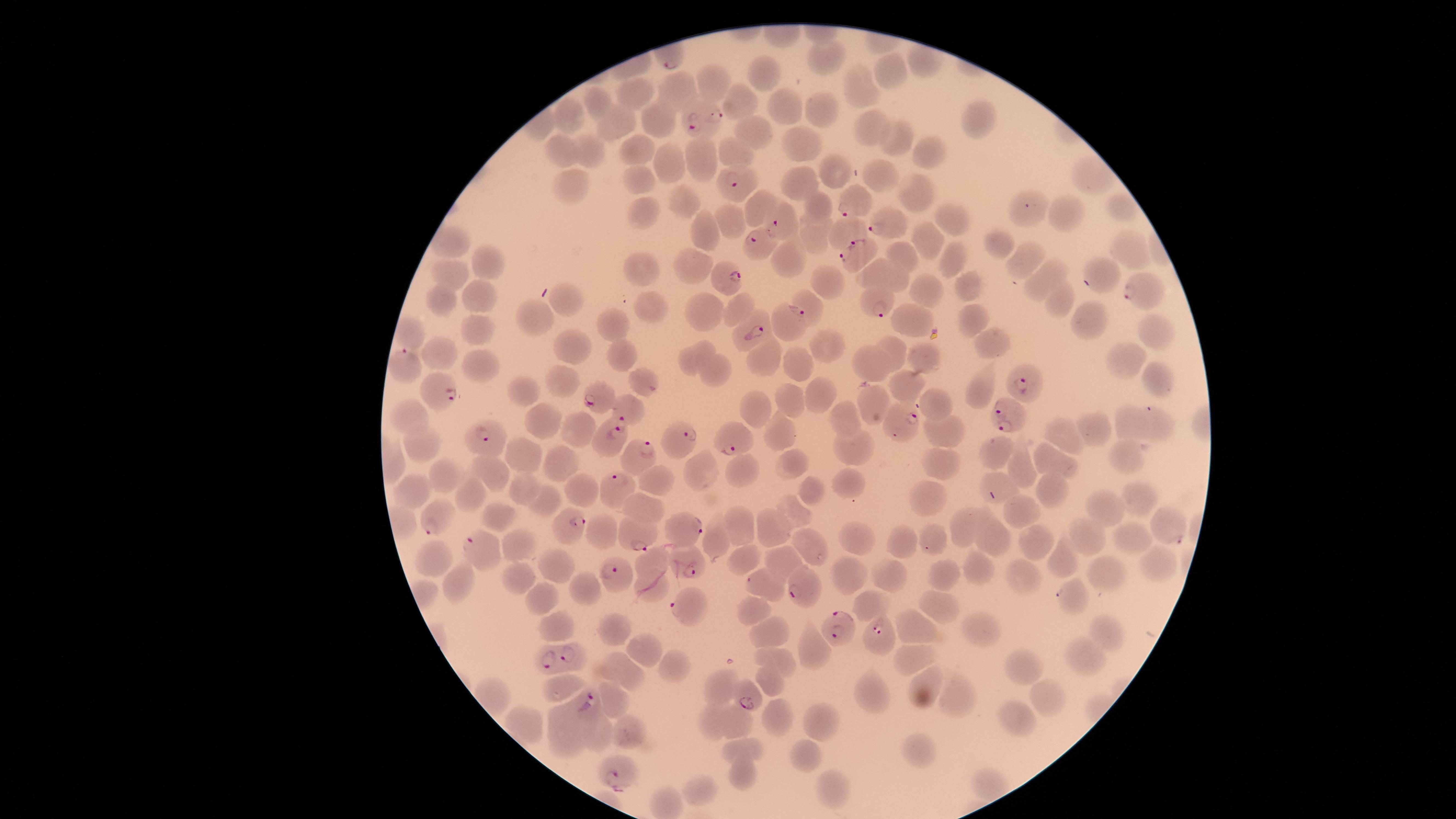 Approximate marker points as [x, y] in pixels. Parasitized RBCs: [703, 124], [738, 178], [850, 202], [783, 225], [887, 226], [755, 238], [857, 249], [728, 276], [1138, 294], [874, 307], [791, 320], [753, 332], [409, 369], [1024, 383], [443, 386], [605, 402], [627, 413], [1003, 419], [902, 420], [613, 435], [733, 439], [487, 440], [684, 442], [641, 457], [618, 482], [436, 521], [567, 524], [690, 531], [1175, 537], [640, 541], [471, 546], [611, 571], [690, 571], [800, 589], [1060, 595], [687, 605], [837, 630], [879, 633], [562, 656], [747, 702], [588, 709], [615, 774]. Uninfected RBCs: [825, 59], [923, 61], [889, 69], [766, 73], [712, 79], [862, 90], [680, 91], [634, 96], [598, 100], [735, 102], [783, 106], [815, 108], [572, 112], [977, 117], [663, 119], [611, 124], [872, 126], [755, 133], [894, 140], [803, 141], [641, 149], [561, 150], [586, 150], [923, 150], [733, 152], [697, 158], [675, 167], [838, 172], [643, 177], [573, 183], [804, 183], [1095, 183], [917, 189], [676, 199], [760, 206], [817, 206], [1121, 210], [1063, 212], [649, 213], [956, 219], [729, 223], [707, 230], [847, 231], [815, 233], [995, 238], [930, 239], [1123, 247], [1022, 252], [789, 253], [903, 255], [951, 257], [492, 261], [697, 265], [1101, 270], [642, 272], [883, 275], [450, 277], [825, 280], [1037, 281], [965, 287], [921, 288], [484, 293], [443, 300], [1050, 300], [569, 301], [809, 304], [701, 307], [742, 307], [649, 311], [974, 318], [1088, 319], [543, 320], [908, 320], [612, 325], [1151, 326], [479, 332], [411, 333], [992, 341], [825, 346], [894, 346], [575, 349], [925, 352], [443, 353], [627, 357], [691, 359], [765, 361], [1124, 361], [869, 364], [796, 365], [479, 367], [713, 371], [1153, 374], [637, 376], [562, 382], [978, 385], [525, 386], [902, 386], [819, 393], [789, 397], [873, 404], [935, 404], [757, 406], [408, 414], [538, 414], [842, 415], [1131, 422], [1155, 423], [1096, 431], [576, 432], [944, 432], [782, 433], [1062, 435], [420, 446], [852, 447], [514, 454], [998, 454], [1126, 456], [788, 460], [1048, 461], [562, 466], [940, 467], [1023, 469], [701, 470], [744, 470], [493, 471], [443, 475], [848, 481], [992, 481], [662, 482], [416, 484], [809, 488], [466, 489], [583, 490], [1054, 492], [526, 494], [928, 494], [549, 501], [1141, 502], [645, 508], [1107, 510], [794, 512], [1025, 515], [503, 517], [738, 525], [773, 525], [962, 525], [1132, 532], [935, 534], [902, 536], [605, 537], [1086, 537], [718, 540], [858, 541], [997, 541], [1031, 543], [521, 545], [812, 546], [428, 554], [742, 556], [789, 558], [1062, 558], [653, 560], [551, 564], [1154, 568], [974, 570], [947, 574], [843, 576], [890, 576], [1023, 576], [1106, 577], [459, 582], [524, 584], [766, 585], [582, 589], [648, 589], [543, 601], [869, 606], [939, 608], [751, 613], [613, 622], [556, 627], [979, 627], [924, 630], [1106, 634], [773, 637], [646, 647], [817, 651], [780, 657], [914, 657], [1080, 660], [1023, 667], [626, 670], [679, 670], [768, 677], [560, 684], [720, 688], [872, 693], [923, 693], [960, 695], [1047, 695], [619, 700], [776, 714], [1018, 714], [714, 719], [818, 720], [737, 725], [563, 730], [598, 734], [629, 736], [745, 748], [804, 753], [920, 753], [736, 773], [988, 781], [706, 788], [838, 790]. Image is 1456×819 pixels. Smartphone photograph through the microscope eyepiece. Species: Plasmodium falciparum. Thin blood film. Circular visible region. Giemsa stain. One field of view of the specimen. Presence: malaria parasites identified.